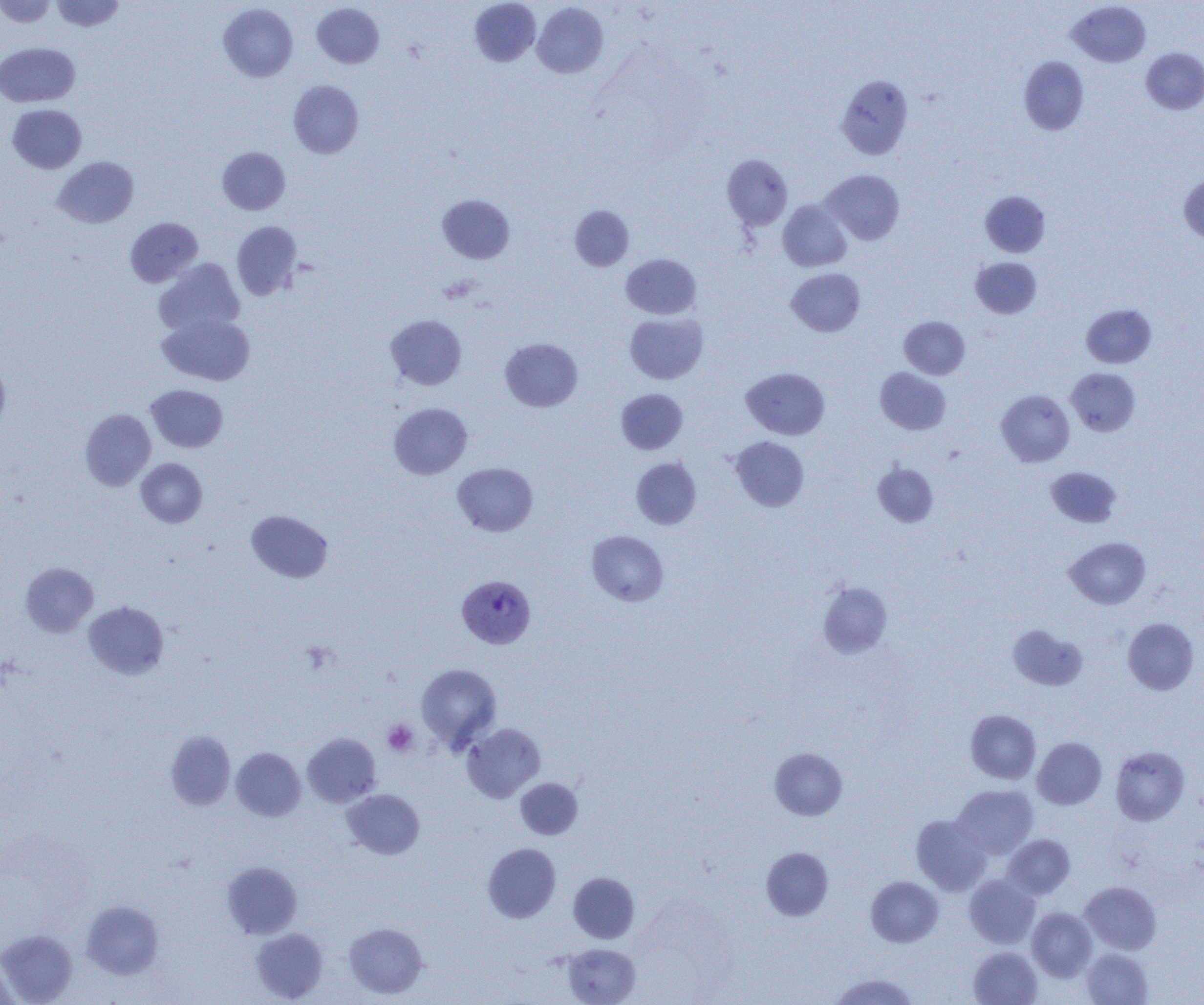
slide_level_diagnosis: Plasmodium vivax
modality: light microscopy
image_size: 1204×1005 pixels
plasmodium_vivax_infected_red_blood_cell_locations: 'approximate bounding boxes as (x1,y1)-(x2,y2) corner pairs in pixels: (457,575)-(536,648)'
field_of_view: one of a larger specimen
magnification: 1000x
preparation: thin blood film
platelet_locations: 'approximate bounding boxes as (x1,y1)-(x2,y2) corner pairs in pixels: (383,720)-(419,756)'
uninfected_red_blood_cell_locations: 'approximate bounding boxes as (x1,y1)-(x2,y2) corner pairs in pixels: (0,0)-(56,27), (52,0)-(125,32), (469,0)-(541,67), (1067,1)-(1151,67), (532,2)-(609,78), (312,3)-(384,69), (218,4)-(298,82), (0,42)-(80,107), (1141,48)-(1204,114), (1019,56)-(1089,135), (836,75)-(914,159), (288,80)-(364,158), (8,104)-(86,173), (217,147)-(290,215), (722,154)-(793,230), (53,156)-(138,228), (821,169)-(905,244), (1179,175)-(1204,245), (980,191)-(1051,257), (437,194)-(515,264), (778,200)-(851,272), (569,205)-(634,271), (125,217)-(203,287), (231,220)-(302,300), (621,254)-(701,319), (970,257)-(1042,318), (154,259)-(245,337), (786,268)-(865,336), (1081,303)-(1156,368), (158,312)-(255,385), (624,312)-(708,384), (385,315)-(467,390), (899,316)-(970,379), (500,338)-(582,412), (0,361)-(10,432), (741,367)-(830,440), (875,367)-(951,435), (1066,368)-(1141,436), (145,384)-(228,452), (616,389)-(688,454), (996,389)-(1075,467), (389,402)-(473,479), (80,409)-(156,490), (730,436)-(810,512), (631,457)-(701,529), (136,458)-(207,527), (453,462)-(538,536), (873,463)-(938,527), (1046,466)-(1121,528), (246,510)-(333,583), (587,530)-(668,606), (1065,537)-(1150,609), (20,562)-(98,637), (817,581)-(893,659), (83,601)-(169,679), (1123,618)-(1199,695), (1007,624)-(1088,690), (415,663)-(502,751), (965,709)-(1041,784), (462,723)-(545,803), (166,730)-(236,810), (302,733)-(381,807), (1032,737)-(1107,809), (1110,746)-(1189,825), (231,747)-(306,821), (770,748)-(847,820), (515,778)-(583,839), (952,784)-(1038,859), (341,789)-(425,859), (911,815)-(990,895), (1002,834)-(1075,900), (483,843)-(561,923), (761,846)-(834,920), (222,861)-(303,939), (568,872)-(640,943), (965,874)-(1040,948), (866,876)-(943,947), (1080,881)-(1161,954), (82,900)-(163,979), (1027,907)-(1097,981), (344,922)-(428,999), (251,928)-(328,1002), (0,929)-(78,1004), (562,943)-(640,1005), (969,947)-(1042,1005), (1081,948)-(1153,1005), (0,954)-(17,1005), (831,973)-(917,1005)'